Outline each blood parasite and name the species.
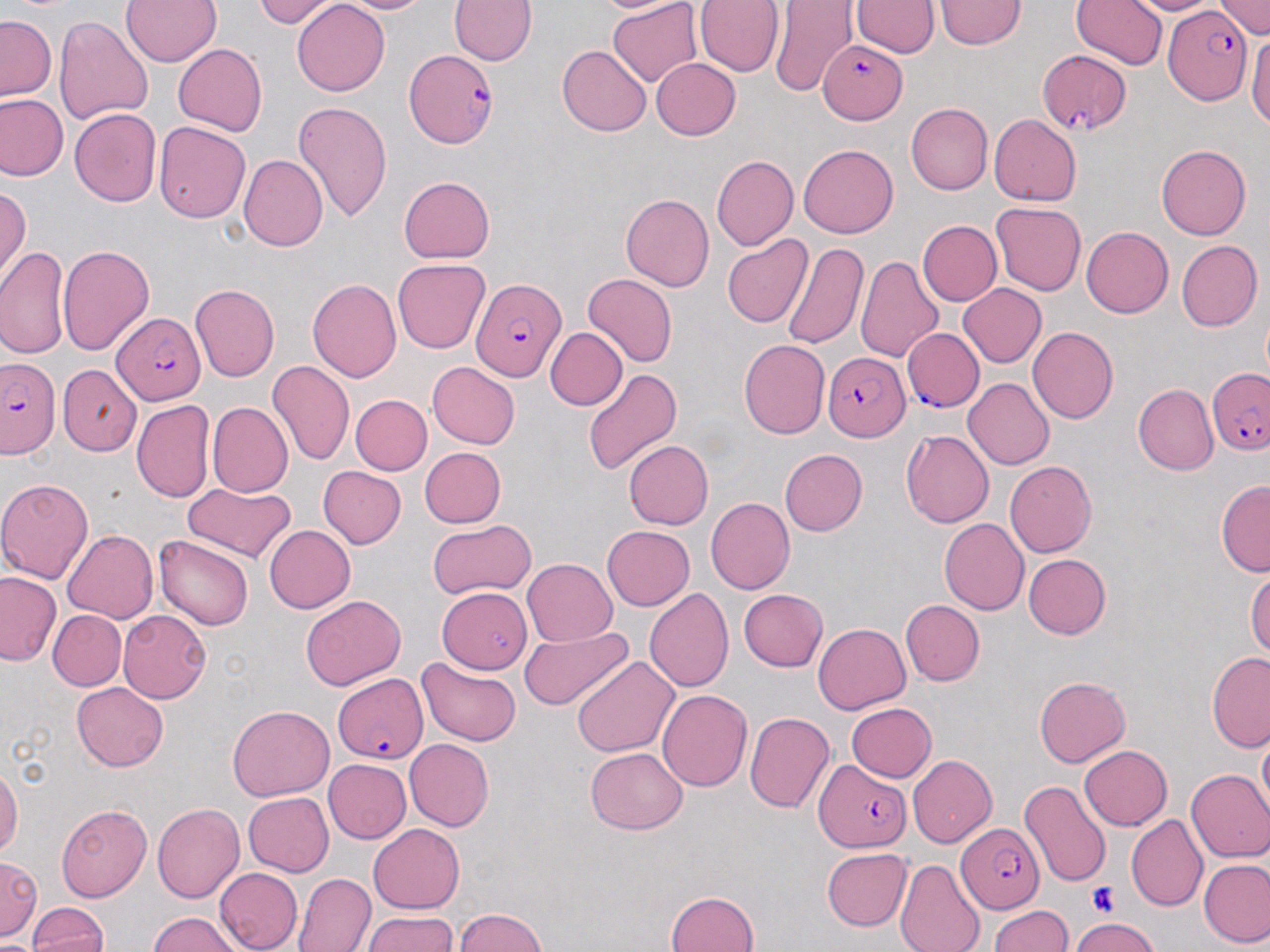

Approximate bounding boxes as [x1, y1, x2, y2] in pixels.
Plasmodium falciparum-infected red blood cells (subset): [1163, 8, 1253, 105], [818, 38, 906, 123], [402, 49, 498, 147], [1039, 49, 1133, 136], [472, 278, 566, 383], [111, 311, 204, 403], [902, 326, 987, 409], [822, 351, 910, 441], [0, 358, 61, 460], [1206, 367, 1270, 455], [333, 675, 427, 764], [813, 758, 910, 852], [955, 822, 1045, 914].
No Plasmodium ovale, Plasmodium malariae, Plasmodium vivax, Babesia divergens, or Trypanosoma brucei observed.

Summary:
  - Uninfected red blood cell locations (subset): [121, 0, 222, 67], [252, 0, 342, 27], [292, 0, 390, 96], [334, 0, 432, 14], [449, 0, 537, 65], [590, 0, 696, 15], [607, 0, 702, 88], [694, 0, 784, 76], [936, 0, 1024, 50], [1072, 0, 1167, 71], [1120, 0, 1219, 15], [1213, 0, 1269, 38], [851, 1, 940, 57], [771, 2, 858, 101], [1, 15, 56, 100], [54, 16, 152, 126], [1247, 32, 1270, 129], [172, 44, 266, 137], [558, 46, 652, 136], [651, 57, 741, 141], [0, 92, 67, 181], [293, 102, 393, 224], [906, 103, 992, 195], [70, 108, 162, 207], [988, 116, 1081, 206], [153, 121, 249, 222], [799, 144, 898, 238], [1156, 144, 1251, 240], [239, 154, 327, 251], [711, 155, 797, 251], [399, 176, 495, 262], [0, 185, 30, 284], [622, 193, 714, 291], [991, 202, 1086, 295], [916, 220, 1002, 306], [1082, 226, 1173, 318], [722, 234, 813, 329], [1176, 240, 1263, 331], [781, 241, 868, 351], [57, 244, 154, 354], [1, 247, 71, 361], [854, 255, 943, 363], [392, 258, 490, 354], [583, 274, 678, 368], [307, 279, 401, 382], [189, 283, 279, 383], [958, 283, 1047, 367], [1028, 327, 1119, 424], [545, 328, 627, 410], [739, 339, 830, 438], [267, 361, 354, 465], [427, 362, 520, 449], [58, 364, 141, 456], [581, 368, 681, 475], [963, 378, 1055, 470], [1132, 384, 1218, 475], [351, 394, 432, 475], [131, 399, 214, 502], [207, 401, 293, 497], [900, 430, 994, 527], [624, 440, 714, 529], [420, 447, 506, 528], [779, 449, 867, 535], [1005, 460, 1097, 557], [318, 466, 406, 548], [0, 478, 95, 583], [1215, 480, 1270, 578], [183, 482, 297, 564], [705, 497, 795, 594], [938, 518, 1029, 615], [428, 519, 537, 600], [263, 525, 355, 613], [602, 525, 694, 610], [63, 529, 158, 623], [153, 534, 255, 631], [1023, 554, 1111, 639], [521, 558, 617, 645], [1247, 564, 1270, 663], [0, 572, 61, 666], [437, 586, 532, 674], [644, 587, 734, 691], [738, 589, 827, 671], [300, 594, 406, 691], [899, 599, 984, 685], [47, 610, 127, 691], [119, 610, 210, 703], [814, 623, 910, 714], [520, 625, 632, 712], [1207, 651, 1270, 752], [572, 655, 678, 757], [417, 657, 521, 746], [413, 660, 506, 830], [1034, 677, 1130, 767], [71, 682, 168, 771], [657, 689, 752, 790], [846, 703, 936, 781], [227, 705, 333, 801], [744, 712, 835, 815], [1258, 732, 1270, 821], [404, 739, 493, 831], [1079, 746, 1172, 830], [585, 747, 688, 833], [909, 755, 997, 847], [323, 758, 412, 843], [0, 766, 21, 857], [1186, 769, 1270, 862], [1019, 779, 1112, 886], [243, 792, 333, 876], [152, 802, 244, 903], [56, 803, 151, 901], [1126, 814, 1208, 911], [369, 823, 464, 914], [821, 847, 912, 930], [895, 858, 986, 952], [1200, 859, 1270, 948], [214, 867, 303, 952], [292, 872, 376, 952], [666, 890, 760, 952], [28, 901, 107, 951], [989, 904, 1073, 952], [455, 908, 548, 952], [362, 911, 457, 951], [150, 912, 243, 951], [1071, 917, 1158, 952]
  - Platelet locations: [1088, 884, 1121, 916]
  - Slide-level diagnosis: Plasmodium falciparum
  - Magnification: 1000x
  - Field of view: one of a larger specimen
  - Stain: May-Grünwald-Giemsa
  - Image size: 1270×952 pixels
  - Preparation: thin blood film
  - Modality: optical microscopy